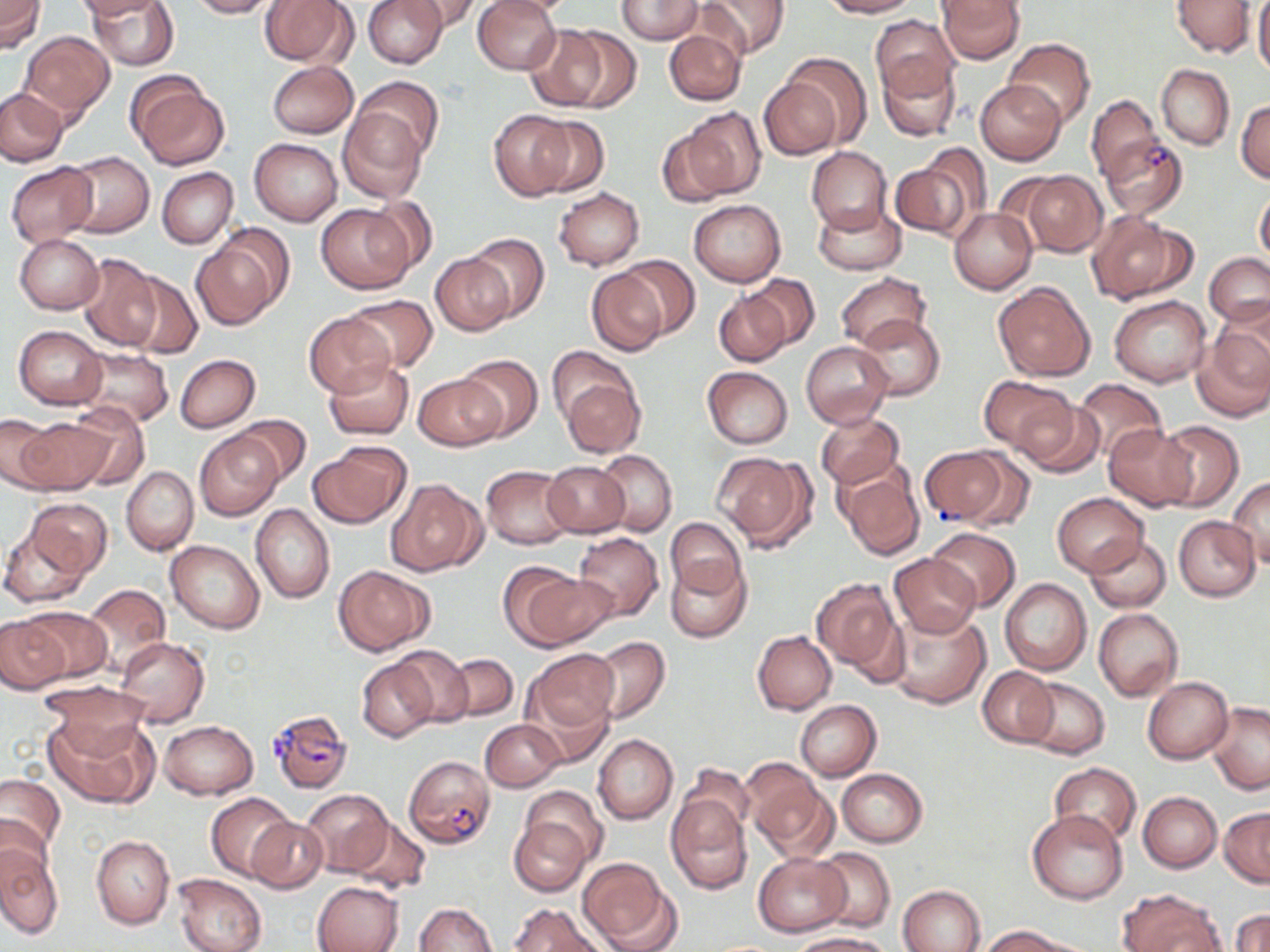 Approximate bounding boxes as named x1/y1/x2/y2 corners in pixels. Uninfected red blood cell locations: (x1=0, y1=0, x2=44, y2=52), (x1=74, y1=0, x2=167, y2=19), (x1=87, y1=0, x2=178, y2=70), (x1=186, y1=0, x2=278, y2=19), (x1=259, y1=0, x2=356, y2=67), (x1=362, y1=0, x2=448, y2=69), (x1=403, y1=0, x2=483, y2=32), (x1=472, y1=0, x2=563, y2=75), (x1=615, y1=0, x2=702, y2=43), (x1=694, y1=0, x2=789, y2=60), (x1=818, y1=0, x2=917, y2=18), (x1=936, y1=0, x2=1025, y2=63), (x1=1170, y1=0, x2=1255, y2=58), (x1=1253, y1=0, x2=1270, y2=79), (x1=869, y1=15, x2=959, y2=104), (x1=529, y1=24, x2=625, y2=112), (x1=663, y1=28, x2=746, y2=105), (x1=19, y1=31, x2=114, y2=123), (x1=1005, y1=39, x2=1095, y2=127), (x1=782, y1=53, x2=872, y2=146), (x1=878, y1=56, x2=960, y2=142), (x1=268, y1=61, x2=359, y2=138), (x1=1156, y1=64, x2=1234, y2=149), (x1=352, y1=76, x2=442, y2=162), (x1=130, y1=77, x2=230, y2=170), (x1=759, y1=78, x2=842, y2=160), (x1=975, y1=79, x2=1066, y2=165), (x1=1, y1=87, x2=69, y2=166), (x1=1086, y1=95, x2=1161, y2=182), (x1=1236, y1=98, x2=1270, y2=183), (x1=338, y1=106, x2=428, y2=202), (x1=680, y1=107, x2=766, y2=200), (x1=488, y1=111, x2=577, y2=202), (x1=528, y1=117, x2=610, y2=196), (x1=655, y1=128, x2=737, y2=209), (x1=250, y1=138, x2=342, y2=225), (x1=806, y1=146, x2=892, y2=235), (x1=63, y1=151, x2=154, y2=238), (x1=893, y1=151, x2=987, y2=243), (x1=6, y1=162, x2=97, y2=247), (x1=157, y1=168, x2=237, y2=249), (x1=1020, y1=172, x2=1106, y2=257), (x1=553, y1=187, x2=645, y2=270), (x1=1255, y1=189, x2=1270, y2=267), (x1=366, y1=195, x2=439, y2=272), (x1=690, y1=200, x2=785, y2=286), (x1=813, y1=201, x2=905, y2=276), (x1=316, y1=203, x2=415, y2=293), (x1=950, y1=208, x2=1037, y2=294), (x1=1086, y1=211, x2=1193, y2=304), (x1=192, y1=228, x2=292, y2=331), (x1=467, y1=234, x2=549, y2=324), (x1=15, y1=235, x2=104, y2=314), (x1=77, y1=252, x2=161, y2=352), (x1=1203, y1=252, x2=1270, y2=326), (x1=430, y1=254, x2=513, y2=336), (x1=615, y1=254, x2=699, y2=338), (x1=585, y1=268, x2=671, y2=356), (x1=124, y1=273, x2=202, y2=360), (x1=746, y1=273, x2=819, y2=348), (x1=835, y1=273, x2=932, y2=351), (x1=992, y1=280, x2=1097, y2=381), (x1=713, y1=290, x2=790, y2=367), (x1=343, y1=294, x2=438, y2=372), (x1=1109, y1=296, x2=1212, y2=388), (x1=304, y1=311, x2=398, y2=398), (x1=853, y1=313, x2=945, y2=401), (x1=1192, y1=323, x2=1270, y2=423), (x1=14, y1=326, x2=107, y2=410), (x1=801, y1=341, x2=892, y2=427), (x1=545, y1=345, x2=636, y2=431), (x1=74, y1=347, x2=174, y2=428), (x1=175, y1=354, x2=260, y2=432), (x1=456, y1=355, x2=541, y2=440), (x1=324, y1=359, x2=413, y2=439), (x1=703, y1=367, x2=793, y2=449), (x1=414, y1=373, x2=504, y2=451), (x1=978, y1=374, x2=1071, y2=452), (x1=561, y1=377, x2=645, y2=458), (x1=1072, y1=379, x2=1167, y2=462), (x1=1014, y1=397, x2=1104, y2=480), (x1=64, y1=402, x2=150, y2=491), (x1=817, y1=412, x2=903, y2=489), (x1=0, y1=414, x2=61, y2=492), (x1=236, y1=414, x2=310, y2=485), (x1=17, y1=416, x2=112, y2=495), (x1=1154, y1=420, x2=1243, y2=510), (x1=1103, y1=424, x2=1198, y2=510), (x1=196, y1=431, x2=283, y2=520), (x1=310, y1=442, x2=408, y2=528), (x1=595, y1=450, x2=677, y2=537), (x1=715, y1=452, x2=815, y2=552), (x1=541, y1=461, x2=630, y2=538), (x1=836, y1=462, x2=926, y2=559), (x1=122, y1=465, x2=198, y2=556), (x1=481, y1=465, x2=575, y2=548), (x1=386, y1=478, x2=487, y2=577), (x1=1228, y1=478, x2=1269, y2=567), (x1=1052, y1=493, x2=1148, y2=576), (x1=25, y1=499, x2=112, y2=579), (x1=251, y1=503, x2=334, y2=603), (x1=1174, y1=516, x2=1260, y2=601), (x1=665, y1=518, x2=747, y2=599), (x1=1, y1=520, x2=95, y2=608), (x1=927, y1=526, x2=1020, y2=611), (x1=573, y1=532, x2=663, y2=621), (x1=1084, y1=534, x2=1171, y2=611), (x1=166, y1=539, x2=265, y2=633), (x1=889, y1=553, x2=980, y2=638), (x1=667, y1=557, x2=750, y2=643), (x1=502, y1=565, x2=614, y2=650), (x1=335, y1=566, x2=432, y2=654), (x1=811, y1=578, x2=904, y2=678), (x1=999, y1=579, x2=1092, y2=675), (x1=82, y1=584, x2=171, y2=676), (x1=18, y1=606, x2=112, y2=683), (x1=888, y1=606, x2=991, y2=709), (x1=1093, y1=608, x2=1182, y2=700), (x1=0, y1=617, x2=70, y2=693), (x1=753, y1=631, x2=837, y2=714), (x1=116, y1=636, x2=209, y2=727), (x1=589, y1=637, x2=670, y2=723), (x1=389, y1=645, x2=474, y2=727), (x1=527, y1=649, x2=619, y2=735), (x1=443, y1=654, x2=517, y2=722), (x1=357, y1=656, x2=439, y2=741), (x1=979, y1=667, x2=1057, y2=746), (x1=1143, y1=676, x2=1233, y2=764), (x1=1020, y1=677, x2=1109, y2=759), (x1=38, y1=682, x2=152, y2=757), (x1=518, y1=685, x2=617, y2=768), (x1=795, y1=700, x2=880, y2=780), (x1=1207, y1=702, x2=1270, y2=794), (x1=46, y1=711, x2=157, y2=809), (x1=481, y1=719, x2=566, y2=792), (x1=159, y1=720, x2=258, y2=800), (x1=593, y1=735, x2=677, y2=824), (x1=742, y1=761, x2=835, y2=860), (x1=1048, y1=763, x2=1141, y2=846), (x1=676, y1=767, x2=755, y2=849), (x1=838, y1=768, x2=927, y2=846), (x1=0, y1=775, x2=65, y2=856), (x1=519, y1=785, x2=608, y2=866), (x1=302, y1=789, x2=392, y2=876), (x1=1137, y1=791, x2=1221, y2=872), (x1=206, y1=792, x2=295, y2=880), (x1=665, y1=796, x2=751, y2=893), (x1=1219, y1=807, x2=1270, y2=887), (x1=1027, y1=809, x2=1128, y2=903), (x1=0, y1=814, x2=51, y2=890), (x1=245, y1=817, x2=327, y2=893), (x1=345, y1=817, x2=430, y2=894), (x1=510, y1=817, x2=590, y2=896), (x1=91, y1=834, x2=174, y2=930), (x1=0, y1=843, x2=62, y2=940), (x1=813, y1=847, x2=896, y2=932), (x1=752, y1=852, x2=852, y2=936), (x1=577, y1=857, x2=678, y2=952), (x1=172, y1=873, x2=267, y2=952), (x1=312, y1=880, x2=403, y2=952), (x1=897, y1=884, x2=985, y2=952), (x1=1118, y1=889, x2=1225, y2=952), (x1=509, y1=902, x2=607, y2=952), (x1=413, y1=903, x2=497, y2=952), (x1=1231, y1=909, x2=1270, y2=952), (x1=978, y1=925, x2=1073, y2=952), (x1=789, y1=933, x2=890, y2=952). Plasmodium falciparum-infected red blood cell locations: (x1=1100, y1=134, x2=1187, y2=219), (x1=918, y1=447, x2=1005, y2=526), (x1=266, y1=709, x2=352, y2=795), (x1=403, y1=754, x2=495, y2=849). Slide-level diagnosis: Plasmodium falciparum. May-Grünwald-Giemsa-stained preparation. 1000x magnification. Thin blood film. One field of a larger specimen. Optical microscopy. Image is 1270×952 pixels.